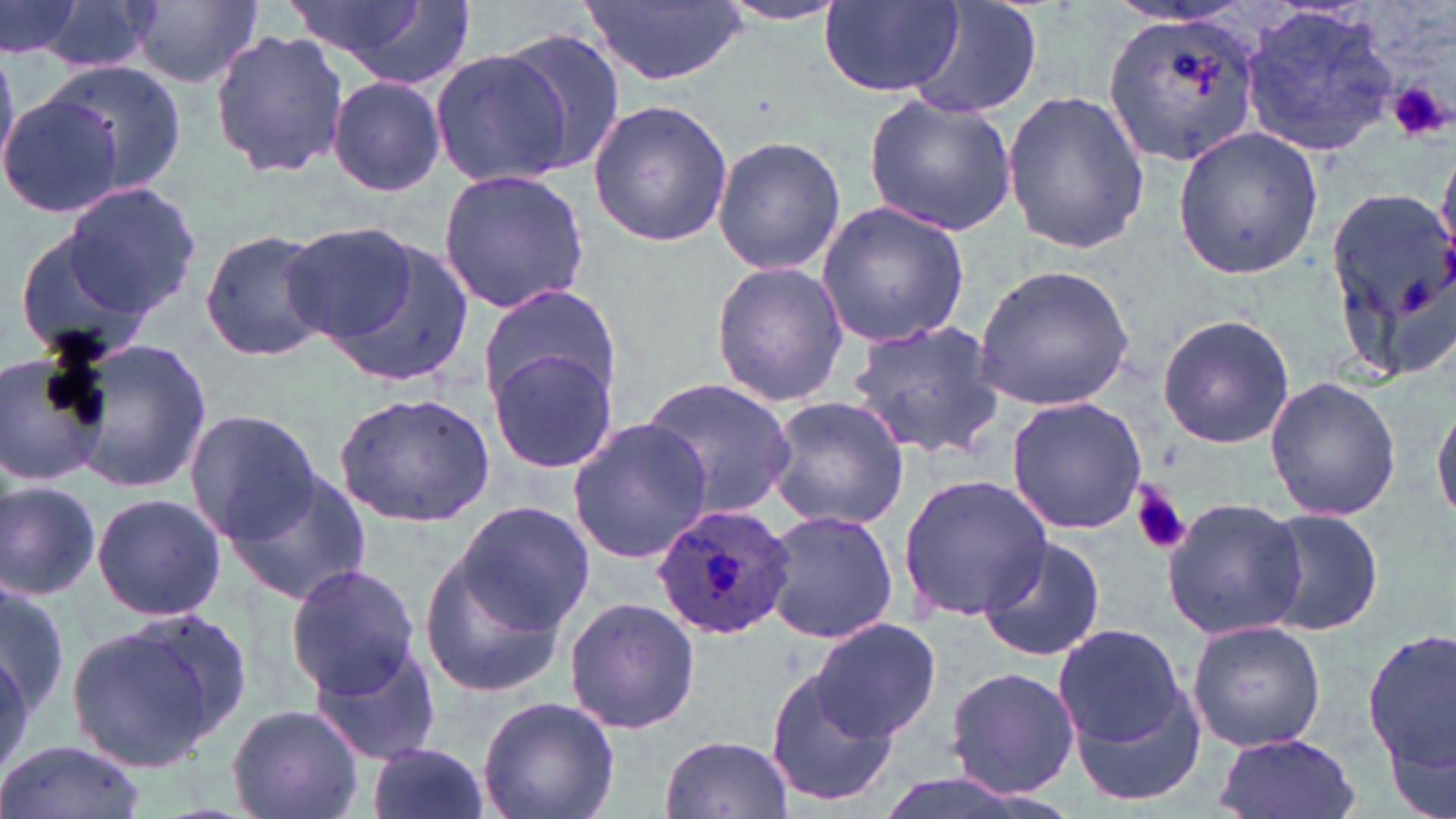
Approximate bounding boxes as (x1,y1)-(x2,y2) corner pairs in pixels. Plasmodium ovale-infected red blood cell locations: (650,503)-(795,640). Uninfected red blood cell locations: (26,0)-(158,73), (281,0)-(462,81), (580,0)-(750,86), (0,1)-(83,62), (128,1)-(261,89), (820,1)-(965,95), (907,1)-(1044,117), (712,3)-(851,27), (1241,4)-(1398,155), (1101,7)-(1263,165), (498,27)-(627,179), (210,29)-(348,178), (430,47)-(569,189), (44,59)-(187,199), (327,75)-(446,198), (1002,89)-(1150,254), (0,90)-(122,218), (863,93)-(1018,235), (588,98)-(734,248), (1171,126)-(1324,279), (709,133)-(847,276), (438,167)-(589,315), (57,180)-(200,321), (1322,183)-(1456,384), (816,201)-(971,349), (280,222)-(418,347), (10,223)-(162,366), (200,228)-(335,362), (316,230)-(476,389), (709,261)-(849,407), (971,263)-(1138,410), (476,283)-(623,415), (1155,313)-(1296,449), (847,319)-(1005,460), (64,339)-(209,495), (484,345)-(621,476), (0,350)-(109,487), (1264,375)-(1402,521), (640,379)-(797,522), (334,392)-(494,526), (766,394)-(912,531), (1006,395)-(1147,534), (1434,396)-(1456,531), (182,409)-(319,542), (567,418)-(712,565), (219,465)-(374,607), (896,473)-(1054,623), (0,482)-(101,601), (91,492)-(226,621), (1161,495)-(1308,642), (456,502)-(593,629), (1256,505)-(1386,639), (762,507)-(898,646), (977,533)-(1106,662), (418,536)-(579,700), (285,563)-(421,698), (0,585)-(68,730), (563,596)-(700,734), (68,613)-(244,770), (811,617)-(942,741), (1187,619)-(1326,754), (1052,623)-(1188,752), (1365,623)-(1456,795), (307,642)-(443,765), (763,663)-(903,809), (941,665)-(1081,799), (1068,676)-(1207,805), (477,695)-(621,819), (227,704)-(365,819), (1210,731)-(1360,819), (659,734)-(796,818), (1,740)-(146,819), (366,741)-(493,819), (864,773)-(1063,819). Platelet locations: (1388,79)-(1449,144), (1131,483)-(1191,554). Slide-level diagnosis: Plasmodium ovale. 1000x magnification. Thin blood film. Light microscopy. Image is 1456×819 pixels. Single field of view. May-Grünwald-Giemsa stain.